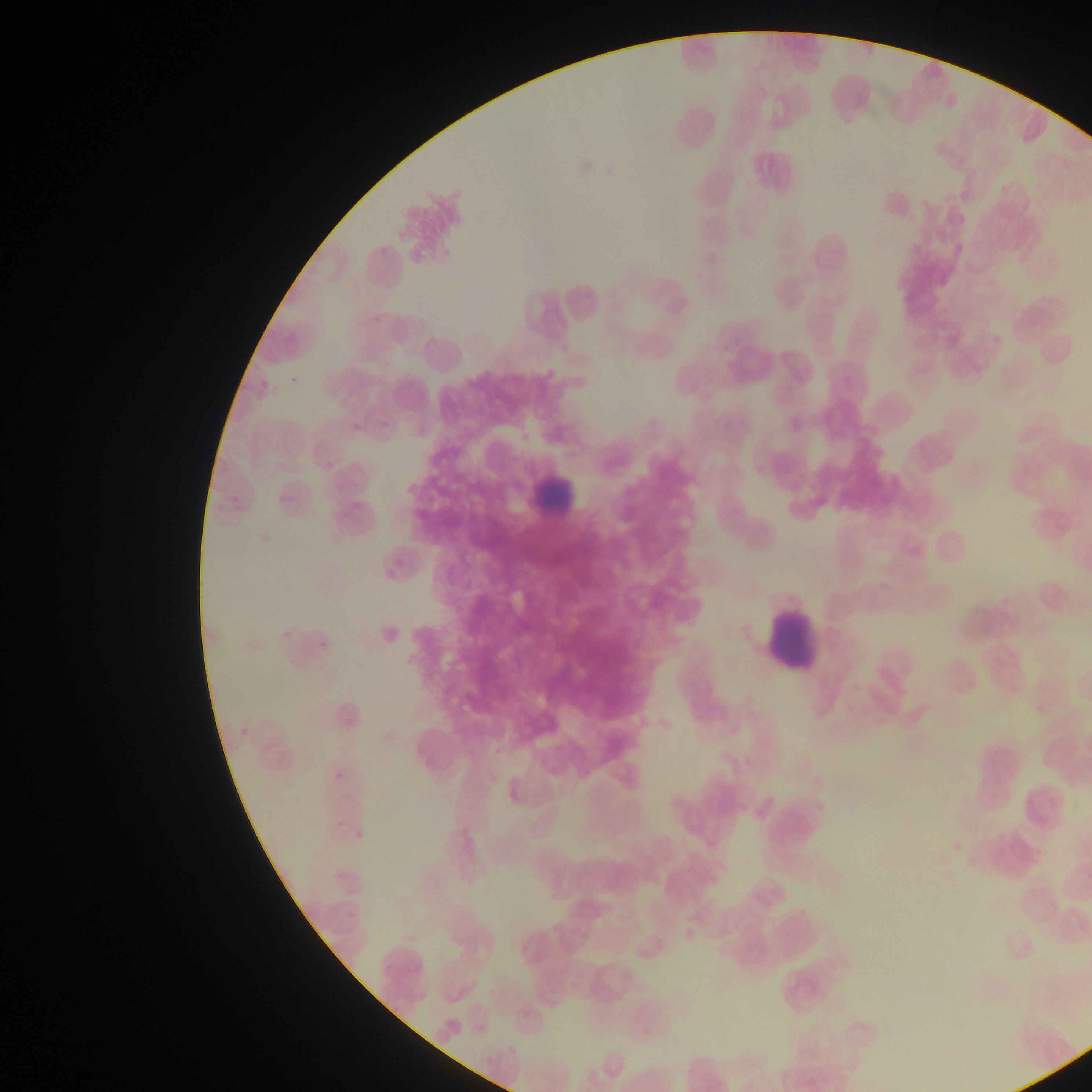 Approximate bounding boxes as (left, top, right, bottom) in pixels. Leukocyte locations: (663, 92, 728, 155), (525, 461, 590, 526), (761, 596, 826, 678). Plasmodium parasite locations: (287, 375, 298, 387), (258, 378, 267, 390), (347, 410, 374, 430), (320, 457, 337, 473), (273, 486, 298, 502), (387, 554, 408, 565), (382, 565, 396, 581), (280, 628, 288, 645), (315, 636, 330, 652), (238, 718, 249, 738), (332, 768, 342, 779), (351, 830, 362, 843). Mobile-phone photograph taken through the microscope. Thin blood film. Image is 1092×1092 pixels. Sample from Ghana. One field of view.